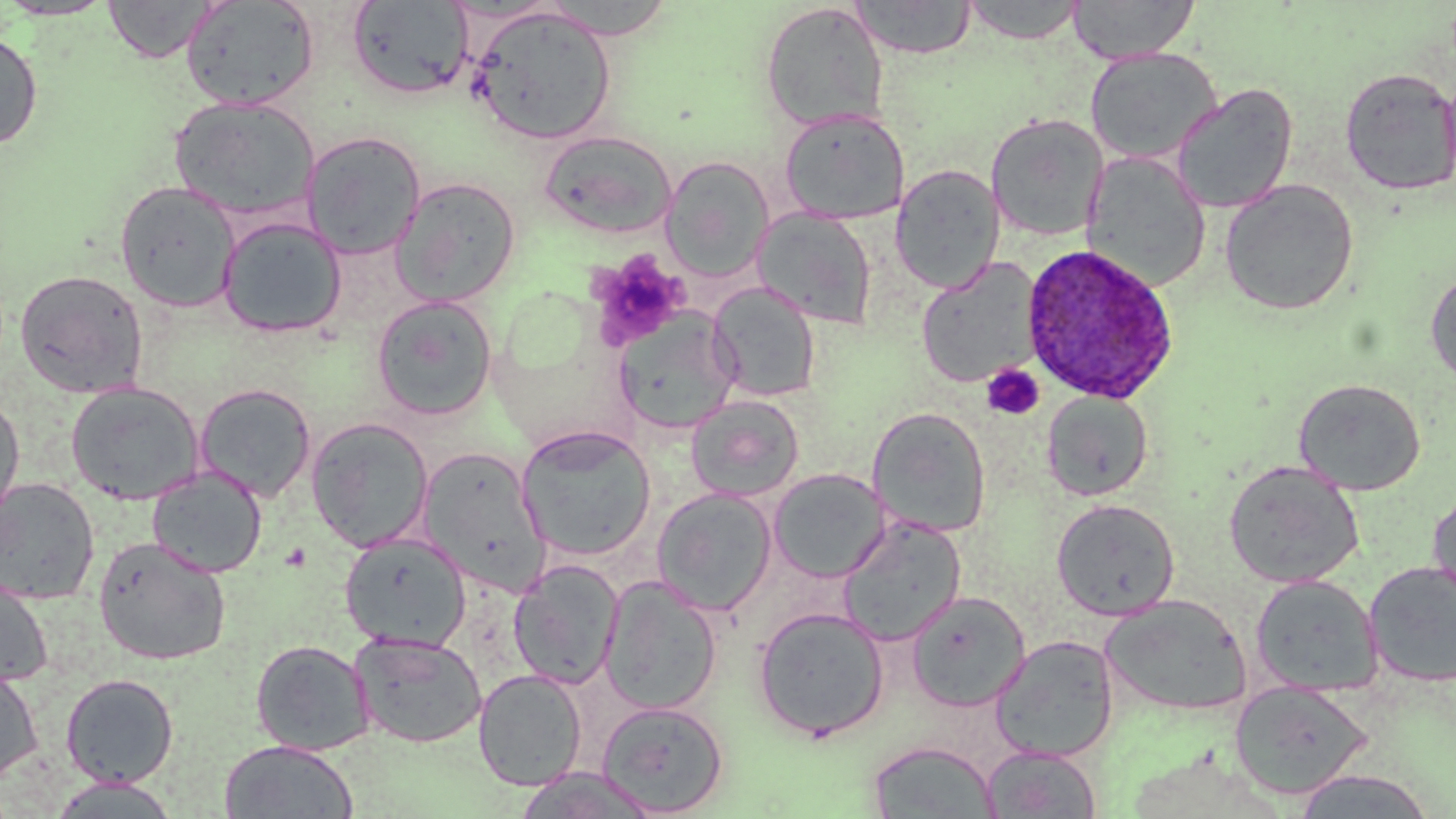

Summary:
  - Coordinate format: approximate bounding boxes as [x1, y1, x2, y2] in pixels
  - Platelet locations: [585, 249, 690, 349], [982, 364, 1044, 420]
  - Uninfected red blood cell locations: [0, 0, 118, 21], [103, 0, 219, 63], [181, 0, 319, 111], [538, 0, 678, 39], [851, 0, 977, 59], [1068, 0, 1200, 63], [346, 1, 474, 100], [961, 1, 1087, 43], [759, 2, 889, 131], [467, 5, 617, 145], [0, 28, 43, 152], [1085, 47, 1223, 164], [1441, 65, 1456, 195], [1339, 67, 1456, 196], [1172, 83, 1298, 213], [169, 96, 320, 222], [779, 109, 909, 224], [985, 113, 1109, 240], [539, 130, 678, 239], [301, 131, 426, 260], [1081, 153, 1211, 291], [661, 155, 774, 281], [890, 164, 1004, 292], [391, 177, 522, 306], [1220, 179, 1359, 315], [114, 180, 240, 312], [753, 207, 878, 330], [217, 216, 347, 338], [916, 259, 1042, 388], [14, 269, 149, 398], [1426, 269, 1456, 386], [708, 281, 821, 402], [371, 295, 497, 420], [614, 310, 741, 434], [1293, 378, 1426, 495], [65, 382, 204, 505], [194, 382, 317, 503], [1041, 390, 1154, 501], [0, 393, 26, 526], [686, 394, 804, 502], [868, 406, 992, 538], [306, 417, 434, 552], [516, 425, 656, 560], [418, 447, 550, 595], [1224, 461, 1364, 588], [147, 466, 267, 578], [769, 468, 890, 582], [0, 478, 100, 604], [652, 488, 778, 616], [1427, 489, 1456, 607], [1051, 498, 1181, 620], [838, 516, 966, 646], [339, 532, 471, 652], [94, 536, 232, 665], [509, 559, 624, 689], [1364, 562, 1456, 687], [0, 572, 54, 688], [1250, 574, 1382, 697], [599, 576, 723, 714], [906, 591, 1030, 712], [1101, 594, 1251, 717], [753, 606, 890, 741], [351, 632, 486, 748], [990, 634, 1120, 762], [250, 639, 375, 756], [0, 664, 43, 787], [473, 669, 587, 790], [60, 673, 179, 787], [1229, 678, 1375, 799], [596, 700, 729, 816], [219, 740, 357, 818], [867, 740, 1000, 818], [982, 744, 1102, 818], [512, 768, 659, 818], [1291, 769, 1437, 818], [47, 776, 182, 817]
  - Plasmodium ovale-infected red blood cell locations: [1020, 243, 1181, 405]
  - Slide-level diagnosis: Plasmodium ovale
  - Magnification: 1000x
  - Modality: optical microscopy
  - Field of view: single
  - Image size: 1456×819 pixels
  - Stain: May-Grünwald-Giemsa
  - Preparation: thin blood smear